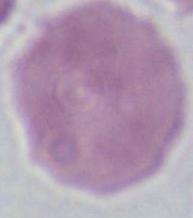

A red blood cell is seen. Micrograph. Captured at 1000x magnification.